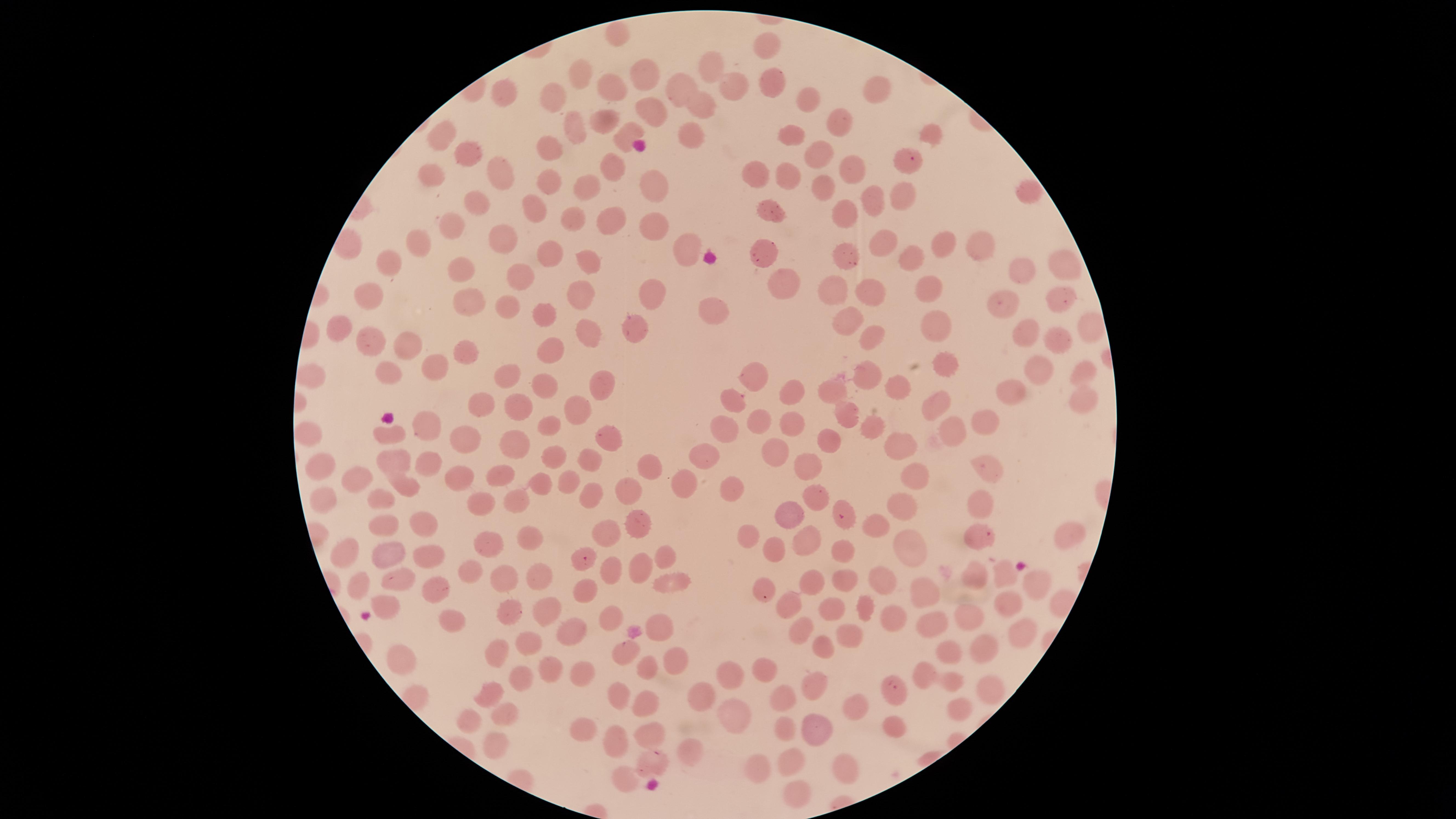
Approximate marker points as {x, y} in pixels.
Summary:
  - Uninfected red blood cells: {616, 35}, {764, 42}, {711, 67}, {584, 76}, {774, 79}, {643, 81}, {613, 87}, {731, 88}, {874, 88}, {682, 89}, {499, 94}, {558, 99}, {810, 99}, {704, 106}, {606, 121}, {842, 121}, {576, 129}, {931, 133}, {624, 134}, {444, 135}, {798, 135}, {691, 138}, {547, 147}, {820, 152}, {472, 155}, {849, 162}, {757, 170}, {500, 171}, {609, 171}, {785, 174}, {433, 175}, {655, 179}, {556, 185}, {818, 188}, {589, 191}, {867, 194}, {1025, 194}, {476, 200}, {901, 200}, {539, 206}, {774, 206}, {846, 209}, {574, 215}, {611, 218}, {650, 218}, {453, 224}, {944, 238}, {973, 241}, {510, 242}, {421, 243}, {679, 243}, {884, 244}, {768, 248}, {844, 250}, {912, 254}, {551, 257}, {392, 260}, {1066, 262}, {590, 264}, {465, 267}, {1025, 271}, {523, 275}, {796, 284}, {931, 285}, {581, 293}, {1062, 293}, {650, 294}, {369, 295}, {832, 295}, {876, 298}, {472, 302}, {1007, 305}, {512, 307}, {714, 310}, {539, 315}, {845, 316}, {937, 320}, {638, 322}, {1085, 322}, {343, 326}, {590, 330}, {1025, 333}, {875, 334}, {371, 339}, {408, 343}, {1061, 345}, {552, 352}, {467, 357}, {944, 364}, {441, 366}, {396, 368}, {1085, 368}, {751, 372}, {1039, 372}, {507, 377}, {870, 379}, {595, 380}, {901, 384}, {548, 385}, {789, 389}, {836, 392}, {731, 393}, {1015, 395}, {1084, 397}, {935, 402}, {483, 403}, {581, 406}, {523, 407}, {848, 416}, {762, 421}, {792, 421}, {548, 423}, {984, 424}, {423, 426}, {720, 427}, {875, 429}, {392, 432}, {309, 433}, {602, 433}, {953, 433}, {465, 436}, {832, 439}, {515, 441}, {898, 441}, {777, 451}, {396, 454}, {551, 455}, {426, 459}, {703, 459}, {589, 460}, {649, 464}, {811, 464}, {320, 472}, {912, 473}, {989, 473}, {498, 475}, {355, 478}, {570, 478}, {457, 479}, {401, 483}, {537, 484}, {684, 484}, {732, 488}, {627, 490}, {816, 493}, {378, 494}, {591, 494}, {318, 499}, {478, 501}, {512, 501}, {980, 503}, {897, 505}, {790, 515}, {383, 523}, {424, 523}, {638, 523}, {879, 529}, {610, 530}, {751, 531}, {1066, 536}, {525, 537}, {804, 538}, {483, 543}, {912, 545}, {774, 547}, {844, 549}, {386, 551}, {343, 552}, {663, 553}, {427, 557}, {642, 563}, {469, 568}, {610, 570}, {975, 571}, {539, 574}, {504, 576}, {1004, 578}, {846, 579}, {880, 579}, {394, 581}, {810, 582}, {1039, 582}, {669, 583}, {355, 584}, {760, 584}, {918, 586}, {434, 588}, {585, 593}, {386, 600}, {1008, 602}, {547, 604}, {787, 604}, {833, 605}, {865, 607}, {512, 609}, {447, 614}, {612, 617}, {888, 618}, {977, 621}, {929, 622}, {659, 625}, {568, 630}, {798, 631}, {1021, 631}, {846, 634}, {526, 641}, {824, 645}, {983, 645}, {953, 648}, {498, 652}, {628, 652}, {672, 655}, {400, 662}, {765, 668}, {579, 669}, {548, 672}, {646, 672}, {924, 672}, {730, 674}, {953, 678}, {816, 679}, {516, 680}, {989, 684}, {623, 693}, {488, 694}, {693, 697}, {785, 698}, {645, 704}, {957, 705}, {848, 706}, {737, 713}, {503, 714}, {470, 716}, {588, 724}, {784, 725}, {890, 725}, {816, 731}, {653, 733}, {617, 738}, {493, 742}, {688, 753}, {791, 758}, {840, 766}, {755, 768}, {624, 776}, {793, 792}
  - Parasitized red blood cells: {909, 158}, {841, 517}, {987, 534}, {582, 559}, {894, 687}, {656, 757}
  - Stain: Giemsa
  - Preparation: thin smear of blood
  - Species: Plasmodium falciparum
  - Field of view: single
  - Capture: smartphone photograph through the microscope eyepiece
  - Presence: malaria parasites detected
  - Visible region: circular
  - Image size: 1456×819 pixels